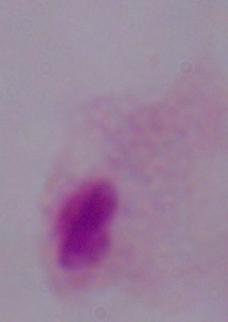 A trichomonad is shown. 1000x magnification. Photomicrograph.